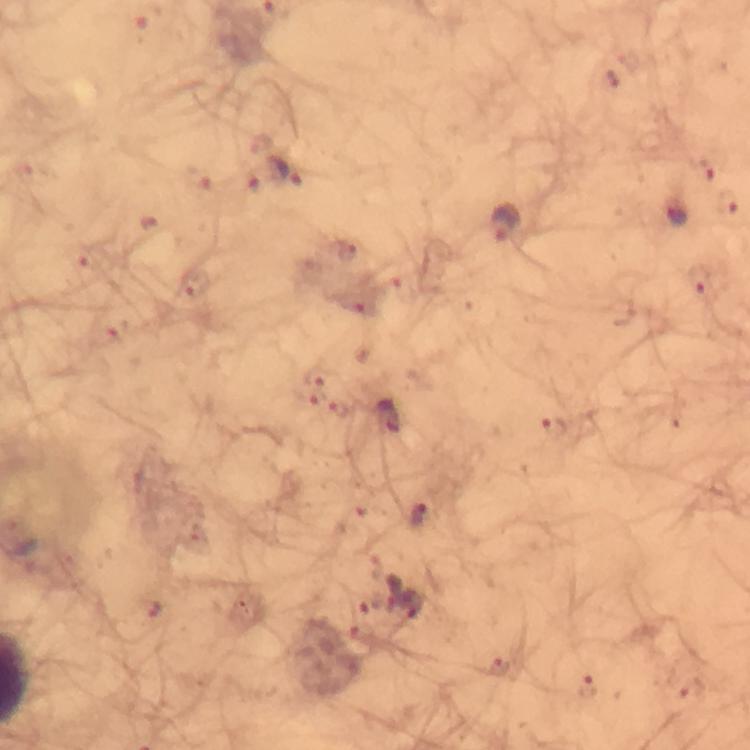

cropped_from: one field of view
magnification: 100x
immersion_oil: used
stain: Giemsa
preparation: thick smear
plasmodium_parasite_locations: 'approximate centers as (x, y) in pixels: (707, 165), (24, 171), (284, 172), (247, 181), (729, 204), (676, 213), (505, 223), (347, 252), (84, 259), (698, 278), (194, 283), (353, 303), (104, 335), (316, 372), (308, 394), (342, 409), (388, 416), (553, 426), (419, 516), (151, 609), (500, 668), (586, 688), (692, 691)'
image_size: 750×750 pixels
capture: smartphone camera through the microscope
context: from a malaria diagnostic workup